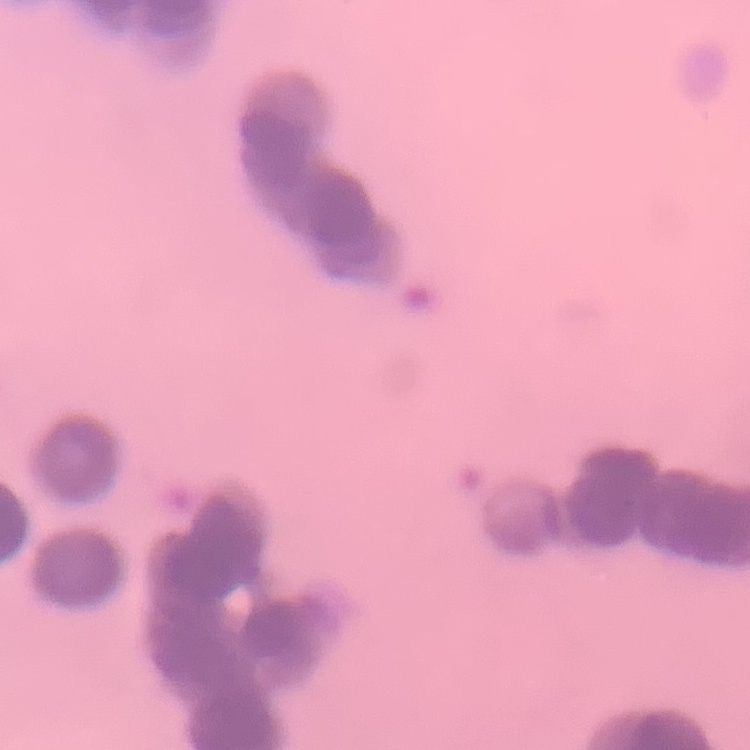

erythrocyte_morphology: rouleaux formation
image_type: square crop of a larger photomicrograph
preparation: thin peripheral smear
stain: Field's or Giemsa